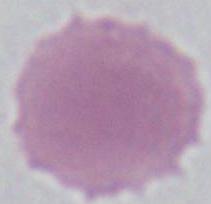

identification = red blood cell
modality = micrograph
magnification = 1000x